Report the malaria status.
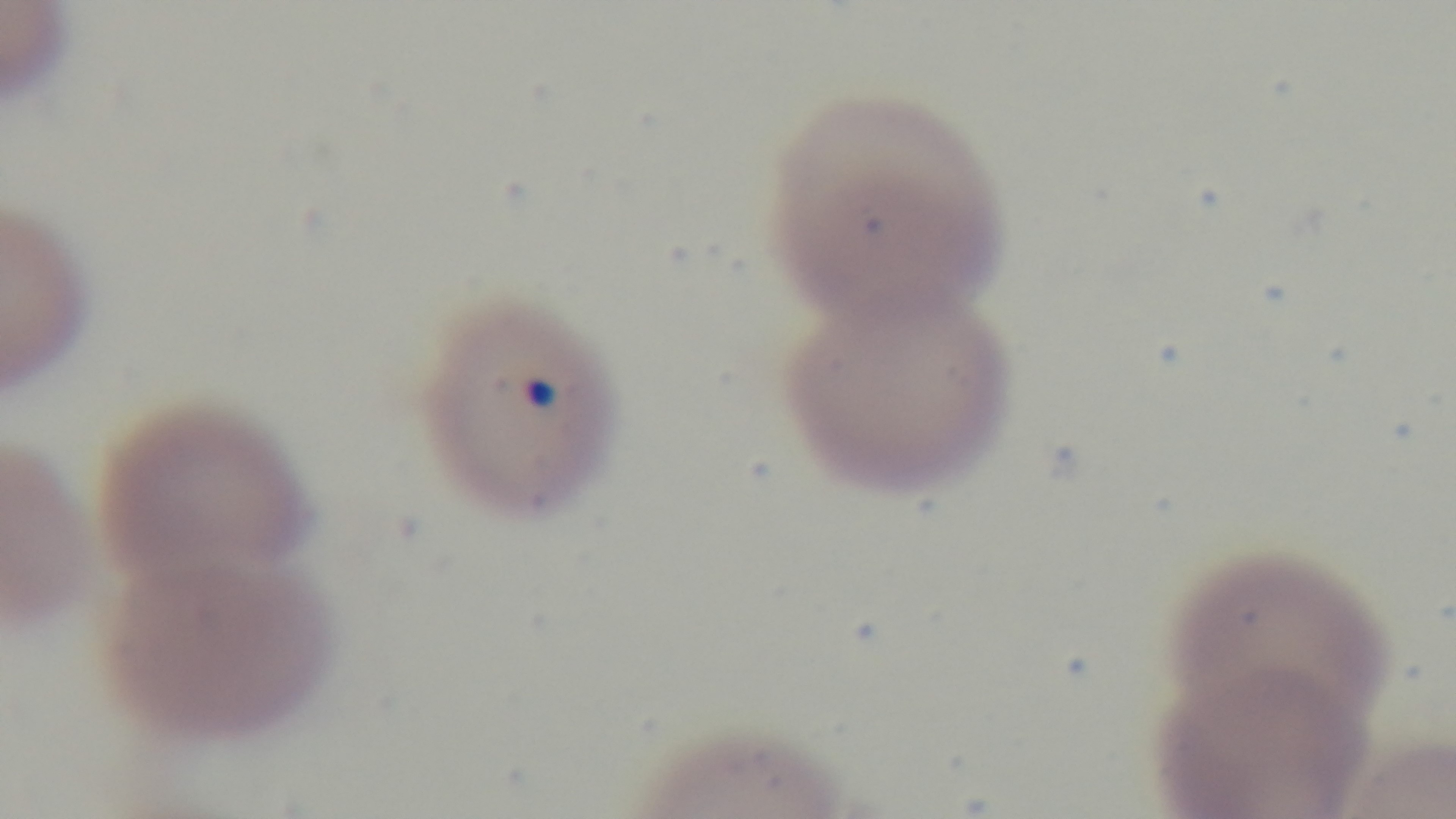

Positive.

stain = Giemsa
field of view = one from the slide
capture = mounted 4K digital camera
objective = 100x oil immersion
preparation = thin smear
modality = light microscopy